Identify the blood parasite species.
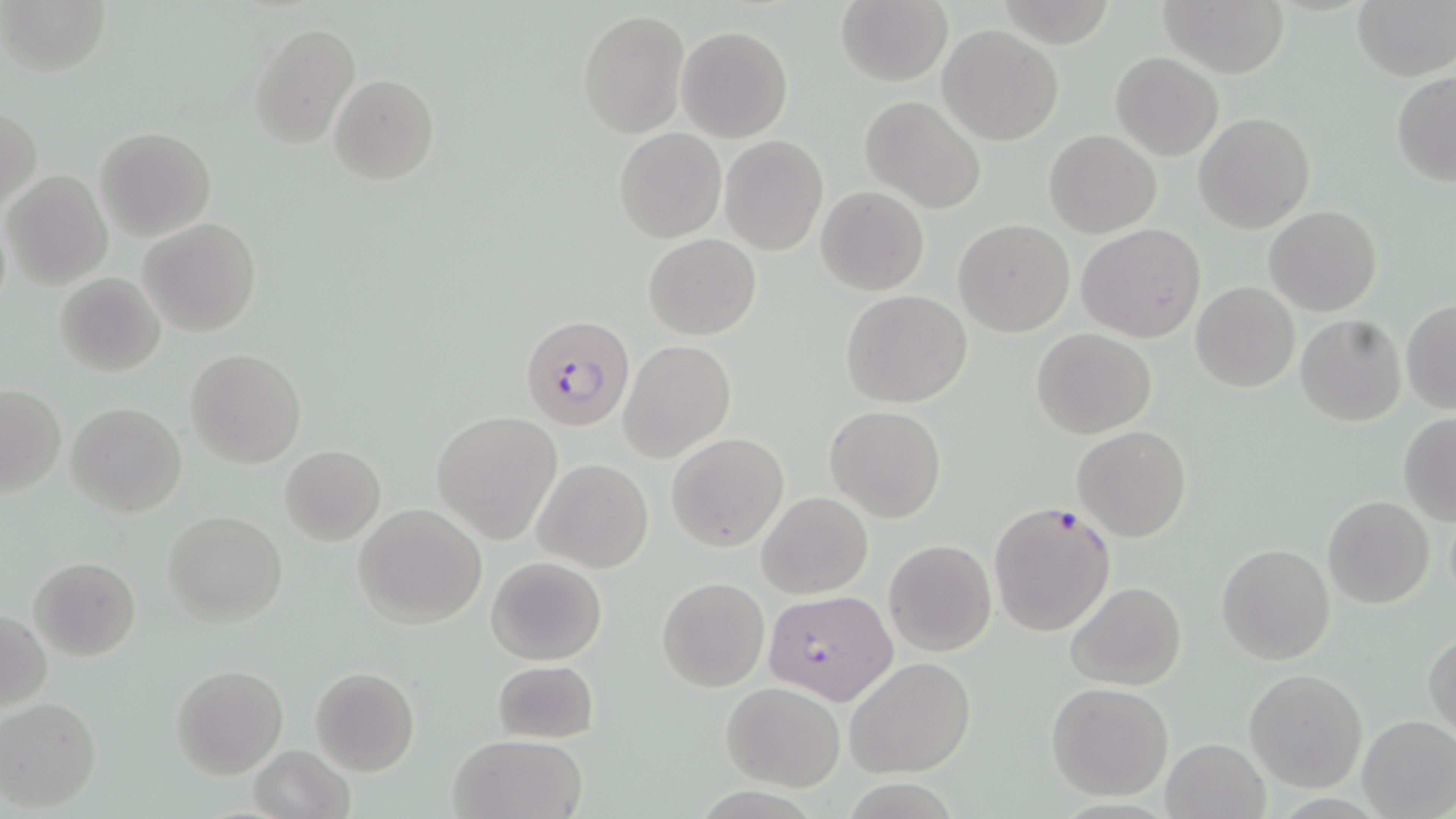
Plasmodium falciparum.

Summary:
  - Coordinate format: approximate bounding boxes as [x1, y1, x2, y2] in pixels
  - Plasmodium falciparum-infected red blood cell locations: [519, 313, 635, 435], [986, 499, 1117, 638], [764, 590, 895, 705]
  - Uninfected red blood cell locations: [3, 0, 113, 76], [1161, 0, 1287, 77], [1351, 0, 1456, 82], [835, 1, 951, 86], [576, 9, 689, 139], [249, 20, 359, 148], [677, 25, 794, 143], [940, 25, 1062, 145], [1111, 51, 1224, 161], [1392, 71, 1455, 186], [329, 73, 440, 186], [859, 95, 985, 213], [1, 107, 40, 214], [1194, 112, 1314, 234], [95, 125, 215, 239], [614, 128, 724, 242], [1045, 129, 1159, 236], [719, 135, 829, 257], [2, 169, 112, 289], [816, 186, 929, 295], [1264, 205, 1382, 315], [139, 217, 261, 337], [954, 219, 1074, 336], [1076, 224, 1205, 344], [643, 234, 760, 339], [55, 272, 167, 377], [1191, 283, 1300, 394], [841, 291, 971, 408], [1401, 300, 1455, 414], [1296, 315, 1406, 425], [1033, 329, 1156, 439], [619, 339, 735, 462], [187, 347, 306, 468], [0, 384, 65, 497], [65, 401, 186, 518], [824, 405, 947, 524], [432, 410, 564, 544], [1398, 412, 1456, 525], [1073, 425, 1191, 541], [667, 432, 787, 552], [280, 446, 385, 544], [532, 459, 654, 572], [758, 491, 872, 598], [1322, 494, 1434, 609], [354, 503, 487, 626], [162, 510, 287, 625], [884, 539, 997, 655], [1216, 543, 1335, 665], [28, 556, 141, 660], [486, 557, 606, 666], [656, 576, 770, 692], [1066, 581, 1185, 691], [1, 610, 50, 711], [1424, 630, 1455, 740], [844, 656, 977, 779], [491, 659, 599, 744], [171, 664, 287, 778], [310, 667, 420, 775], [1244, 669, 1367, 791], [720, 682, 844, 792], [1046, 682, 1173, 801], [0, 697, 101, 811], [1358, 715, 1456, 816], [448, 733, 586, 819], [1161, 738, 1269, 818], [249, 745, 354, 819]
  - Preparation: thin blood film
  - Field of view: single
  - Stain: May-Grünwald-Giemsa
  - Magnification: 1000x
  - Image size: 1456×819 pixels
  - Modality: optical microscopy